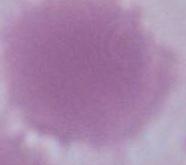

modality: micrograph
identification: red blood cell
magnification: 1000x